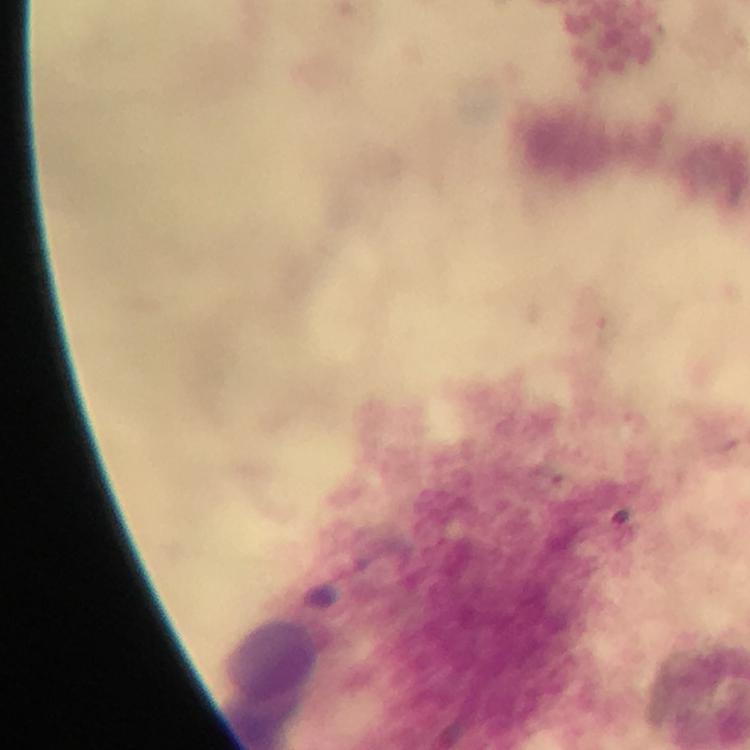
Approximate centers as [x, y] in pixels. Leukocyte locations: [272, 660]. Image is 750×750 pixels. Thick blood film. Photographed through the microscope with a smartphone camera. Giemsa stain. Immersion oil was used. From a malaria diagnostic workup. At 100x magnification. Plasmodium parasites: none seen. Cropped region of a single field of view.